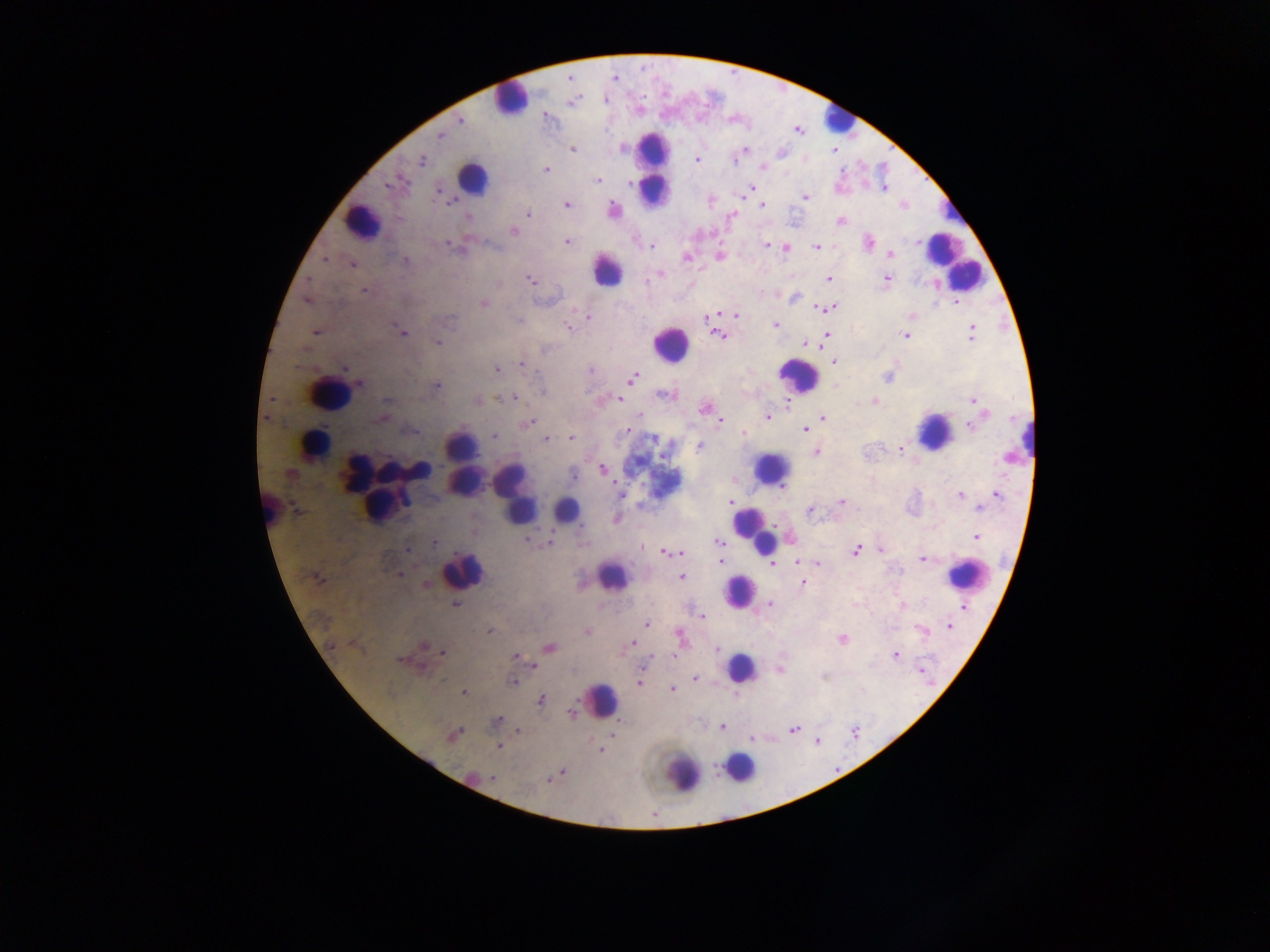
Approximate centers as [x, y] in pixels.
Summary:
  - Malaria parasite locations: [460, 120], [440, 135], [572, 150], [743, 150], [736, 157], [697, 160], [422, 161], [763, 166], [545, 169], [597, 180], [394, 183], [751, 188], [884, 188], [439, 191], [806, 196], [567, 205], [762, 205], [614, 210], [527, 214], [733, 215], [468, 217], [839, 222], [513, 230], [567, 241], [868, 242], [448, 244], [767, 245], [816, 246], [650, 247], [785, 247], [890, 255], [719, 256], [686, 258], [324, 259], [406, 260], [351, 264], [660, 275], [887, 278], [530, 279], [828, 279], [365, 291], [795, 297], [829, 300], [955, 302], [483, 304], [826, 309], [736, 315], [588, 317], [707, 318], [450, 320], [775, 325], [567, 328], [314, 332], [401, 333], [971, 333], [717, 335], [904, 335], [826, 337], [438, 342], [804, 344], [545, 349], [834, 362], [521, 364], [344, 368], [496, 369], [591, 369], [888, 376], [632, 378], [360, 383], [436, 386], [665, 395], [514, 397], [619, 398], [386, 400], [479, 400], [875, 401], [973, 401], [704, 409], [640, 416], [767, 416], [823, 417], [383, 418], [530, 421], [720, 421], [970, 426], [804, 429], [628, 431], [744, 434], [494, 436], [546, 438], [570, 438], [654, 439], [699, 447], [901, 448], [816, 452], [1008, 458], [603, 469], [290, 475], [573, 476], [621, 494], [960, 495], [996, 495], [730, 501], [842, 502], [980, 508], [810, 511], [976, 537], [527, 541], [434, 542], [550, 542], [718, 542], [643, 547], [407, 550], [881, 550], [855, 551], [666, 553], [680, 553], [721, 553], [922, 559], [720, 561], [798, 562], [817, 564], [772, 565], [400, 575], [682, 577], [315, 578], [803, 583], [426, 584], [769, 604], [456, 605], [902, 605], [963, 608], [702, 616], [646, 624], [950, 626], [922, 630], [490, 631], [587, 631], [680, 637], [842, 639], [633, 643], [332, 645], [424, 645], [550, 648], [718, 650], [443, 653], [895, 654], [516, 656], [399, 659], [535, 666], [782, 670], [921, 670], [695, 679], [512, 682], [639, 683], [672, 689], [463, 692], [540, 700], [572, 713], [497, 721], [722, 728], [519, 730], [793, 730], [452, 735], [817, 741], [499, 746], [601, 751], [561, 773], [493, 778], [549, 779]
  - Leukocyte locations: [510, 99], [836, 119], [653, 167], [472, 178], [951, 212], [361, 220], [952, 260], [608, 270], [963, 275], [670, 343], [798, 375], [328, 393], [934, 430], [1027, 439], [462, 442], [312, 444], [771, 468], [422, 470], [464, 479], [377, 492], [513, 492], [381, 504], [268, 505], [562, 512], [754, 530], [463, 570], [965, 574], [612, 577], [741, 590], [741, 667], [602, 700], [740, 767], [683, 773]
  - Capture: mobile-phone photograph through a microscope
  - Country: Ghana
  - Field of view: single
  - Preparation: thick blood film
  - Image size: 1270×952 pixels